Name the parasite shown.
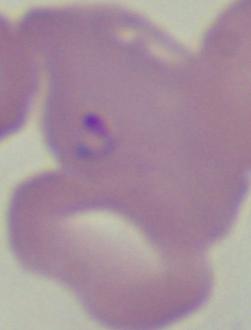
This is Babesia.

modality: micrograph
magnification: 1000x